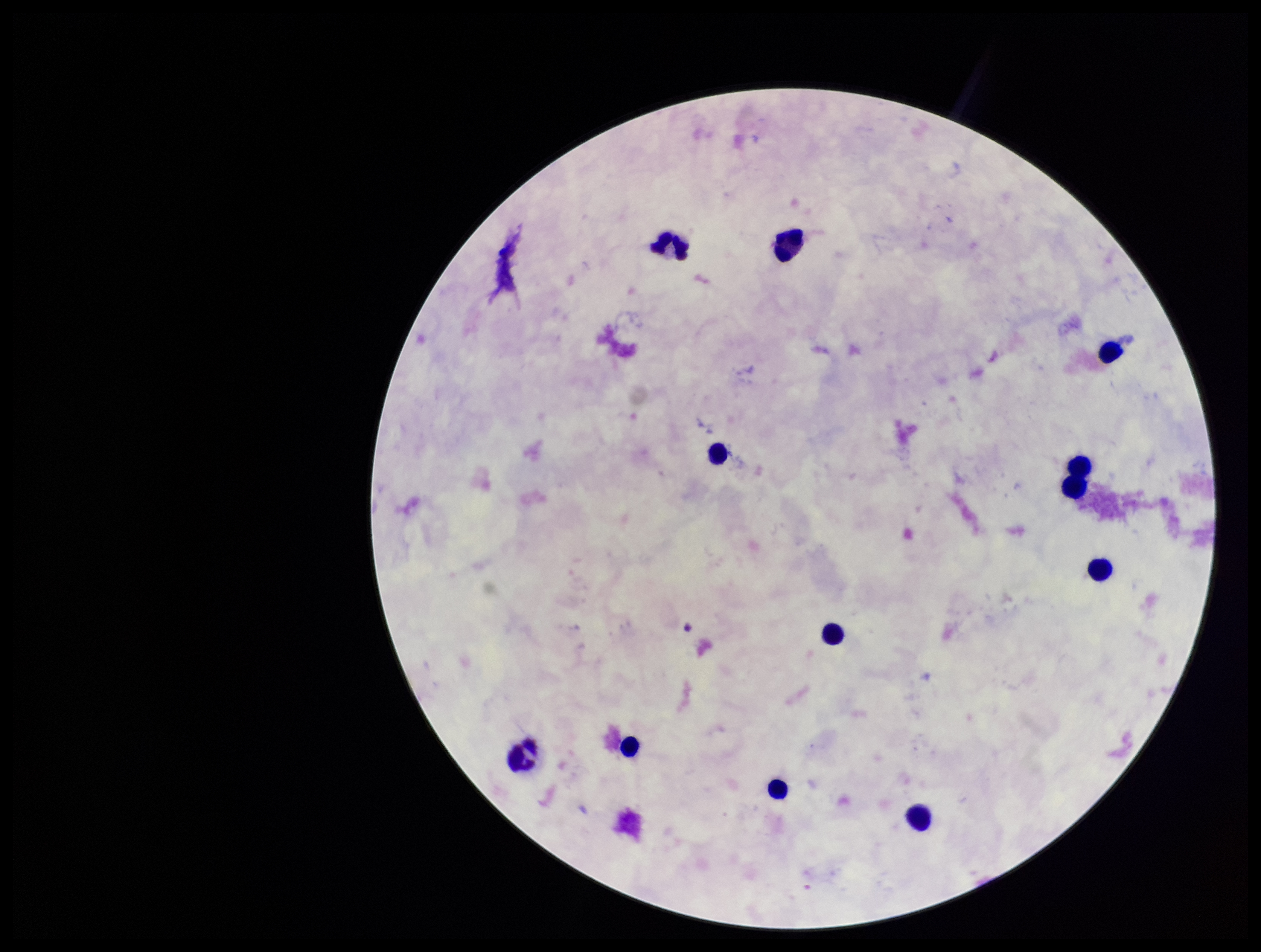
stain: Giemsa
image_size: 1261×952 pixels
leukocyte_count: 11
preparation: thick smear
field_of_view: single
patient_malaria_status: negative
parasite_count: 0
capture: smartphone photograph through the microscope eyepiece
plasmodium_parasites: none identified